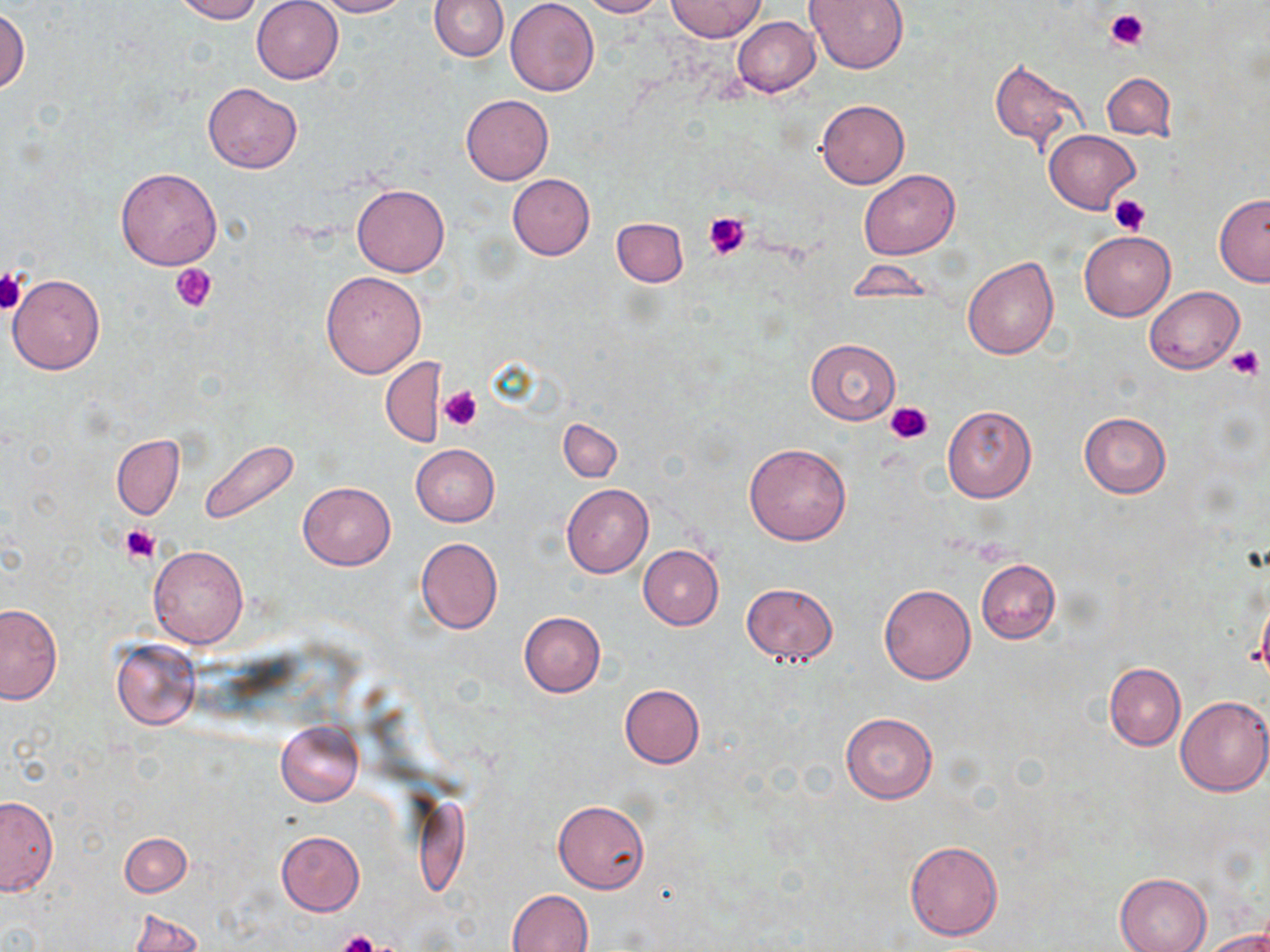
Approximate bounding boxes as [x1, y1, x2, y2] in pixels. Platelet locations: [1106, 8, 1150, 50], [1109, 195, 1154, 235], [702, 211, 751, 259], [172, 263, 216, 313], [0, 267, 26, 315], [1226, 345, 1264, 380], [440, 387, 482, 431], [885, 400, 935, 444], [119, 525, 160, 563], [335, 930, 381, 952]. Uninfected red blood cell locations: [170, 0, 263, 23], [252, 0, 343, 84], [315, 0, 408, 17], [429, 0, 509, 61], [505, 0, 599, 96], [579, 0, 669, 17], [665, 0, 767, 41], [805, 0, 908, 73], [1, 8, 30, 97], [731, 16, 820, 97], [989, 57, 1089, 155], [1102, 72, 1175, 140], [203, 84, 302, 173], [461, 93, 553, 184], [816, 98, 909, 188], [1045, 130, 1140, 213], [115, 167, 222, 269], [858, 170, 960, 260], [507, 174, 595, 260], [352, 184, 449, 276], [1214, 194, 1270, 286], [612, 216, 687, 287], [1079, 230, 1176, 321], [962, 256, 1059, 360], [847, 259, 936, 301], [321, 270, 427, 377], [8, 272, 106, 375], [1145, 285, 1244, 374], [805, 339, 901, 423], [380, 356, 447, 448], [941, 404, 1037, 503], [1078, 413, 1170, 498], [559, 418, 623, 482], [112, 436, 184, 519], [200, 439, 301, 525], [743, 443, 851, 546], [410, 444, 500, 526], [298, 483, 394, 569], [561, 484, 653, 577], [414, 537, 503, 634], [638, 545, 724, 629], [147, 546, 249, 649], [976, 559, 1060, 643], [741, 582, 837, 666], [878, 584, 976, 684], [1255, 589, 1270, 690], [0, 604, 62, 704], [518, 611, 605, 698], [111, 638, 201, 730], [1104, 662, 1185, 751], [620, 684, 704, 768], [1176, 696, 1270, 796], [840, 713, 937, 803], [275, 721, 363, 806], [1, 795, 58, 895], [553, 800, 650, 893], [276, 830, 364, 916], [120, 832, 191, 896], [904, 840, 1002, 940], [1114, 873, 1212, 952], [507, 889, 594, 952], [126, 909, 203, 952], [1204, 928, 1270, 952]. Slide-level diagnosis: negative for blood parasites. May-Grünwald-Giemsa stain. 1000x magnification. Thin blood smear. Single field of view. Image is 1270×952 pixels. Light microscopy.